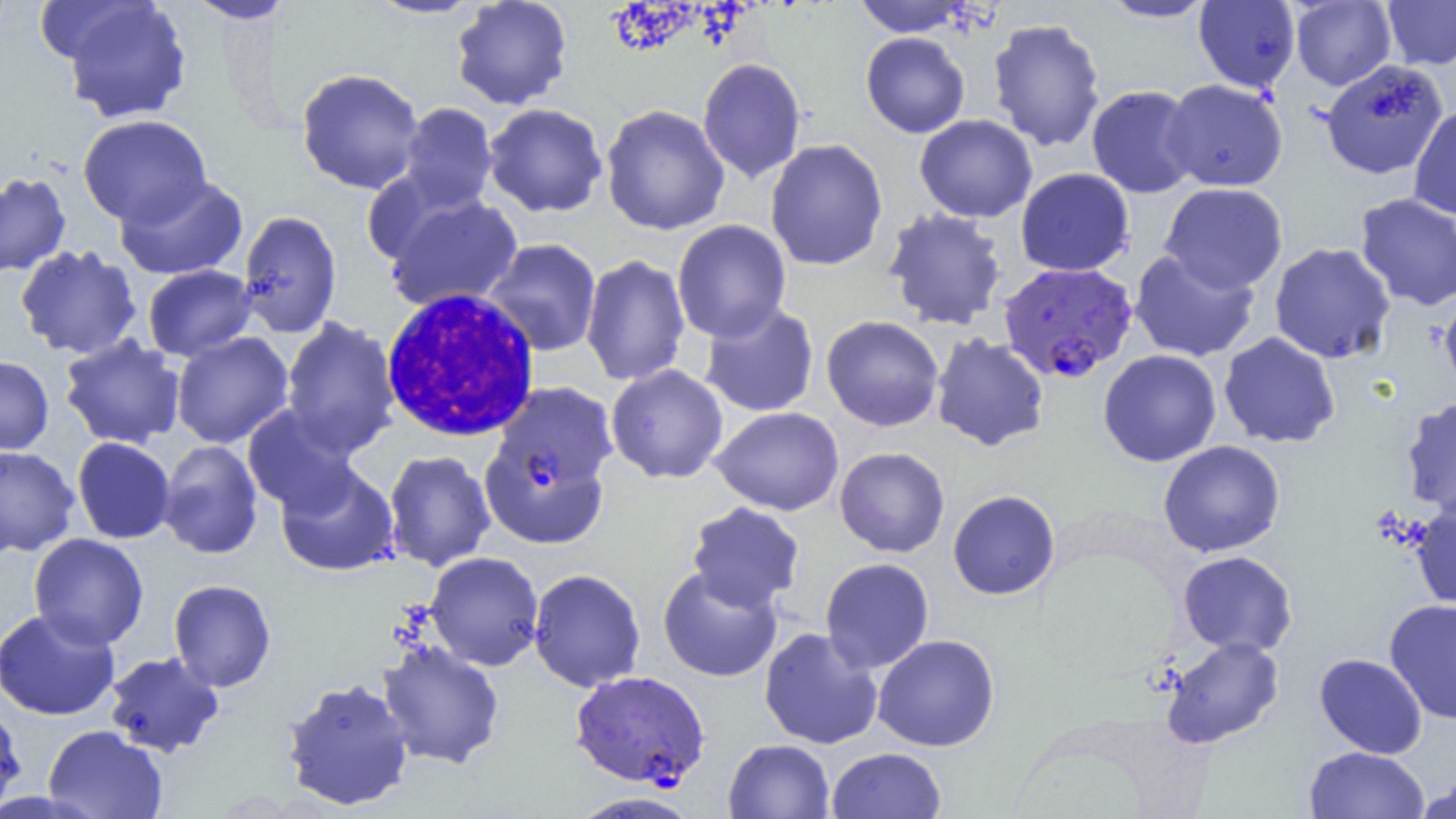

slide-level diagnosis = Plasmodium falciparum
preparation = thin blood smear
Plasmodium falciparum-infected red blood cell locations = approximate bounding boxes as (x1,y1)-(x2,y2) corner pairs in pixels: (997,260)-(1137,384), (484,380)-(620,495), (570,670)-(710,790)
white blood cell locations = approximate bounding boxes as (x1,y1)-(x2,y2) corner pairs in pixels: (380,288)-(542,443)
field of view = single
image size = 1456×819 pixels
magnification = 1000x
uninfected red blood cell locations = approximate bounding boxes as (x1,y1)-(x2,y2) corner pairs in pixels: (183,0)-(293,24), (365,0)-(486,19), (450,0)-(574,111), (853,0)-(972,37), (1097,0)-(1218,22), (1290,0)-(1396,91), (1382,0)-(1456,70), (54,1)-(192,123), (1194,1)-(1300,93), (987,18)-(1106,152), (860,32)-(970,138), (697,57)-(806,183), (1320,59)-(1449,180), (296,67)-(425,194), (1162,79)-(1289,192), (1086,84)-(1201,199), (397,102)-(498,211), (483,103)-(608,217), (600,104)-(730,236), (1408,104)-(1456,220), (914,114)-(1038,223), (77,115)-(212,227), (765,139)-(888,272), (1015,167)-(1134,276), (0,172)-(71,278), (113,175)-(247,280), (1160,182)-(1288,294), (1354,193)-(1456,311), (383,194)-(524,312), (883,207)-(1007,331), (236,211)-(342,338), (672,219)-(792,343), (483,238)-(602,356), (1268,242)-(1396,364), (15,245)-(142,360), (1129,248)-(1261,362), (580,253)-(691,388), (142,264)-(257,362), (1439,286)-(1456,403), (699,302)-(819,417), (821,315)-(944,432), (280,317)-(400,457), (171,332)-(294,448), (1219,332)-(1341,449), (930,333)-(1050,451), (58,335)-(186,450), (1098,349)-(1222,467), (0,355)-(54,455), (605,364)-(729,484), (1401,397)-(1456,518), (242,405)-(361,516), (710,406)-(845,515), (72,437)-(176,544), (158,440)-(264,559), (1157,440)-(1286,558), (0,445)-(79,557), (834,446)-(950,558), (383,450)-(495,572), (276,463)-(400,577), (479,464)-(612,550), (948,489)-(1061,600), (686,501)-(805,612), (1410,502)-(1456,610), (29,533)-(149,650), (1177,550)-(1298,657), (424,551)-(545,671), (820,557)-(934,674), (657,565)-(783,682), (528,568)-(646,692), (168,579)-(277,692), (1384,599)-(1456,724), (0,606)-(121,721), (759,627)-(884,750), (872,634)-(1000,752), (1160,636)-(1284,749), (377,641)-(505,769), (103,651)-(225,757), (1313,653)-(1428,759), (281,676)-(415,811), (0,701)-(27,818), (43,725)-(168,819), (723,739)-(835,819), (1304,746)-(1430,819), (826,747)-(946,819), (1412,778)-(1456,819), (568,791)-(701,818)
modality = light microscopy